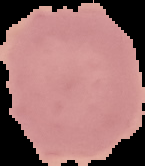 Result: no Plasmodium parasites seen. Image is 145×166 pixels. From a thin blood smear. Cell region segmented out of the field of view; the surrounding area is masked to black.